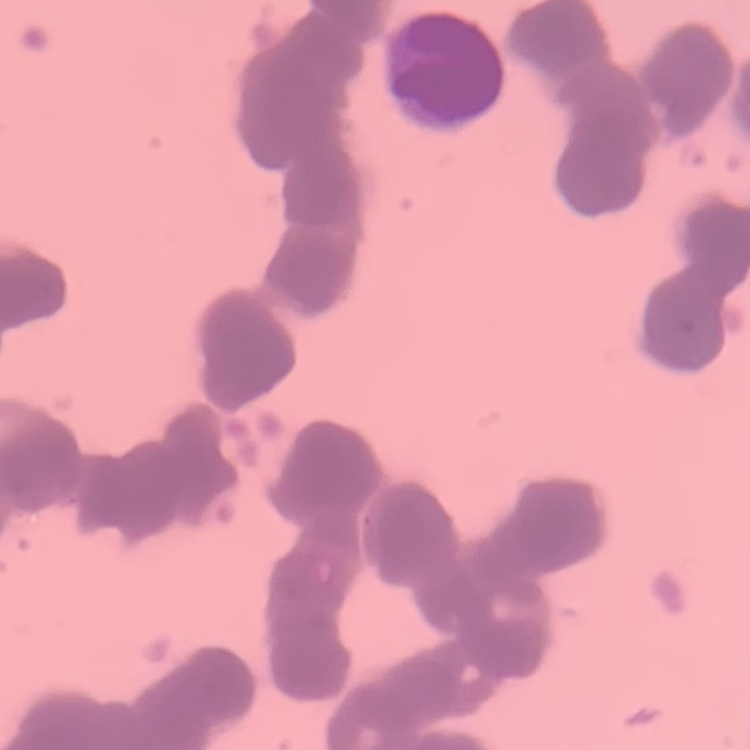

erythrocyte morphology = rouleaux formation
image type = one tile cut from a larger photomicrograph
preparation = thin blood film
stain = Field's or Giemsa